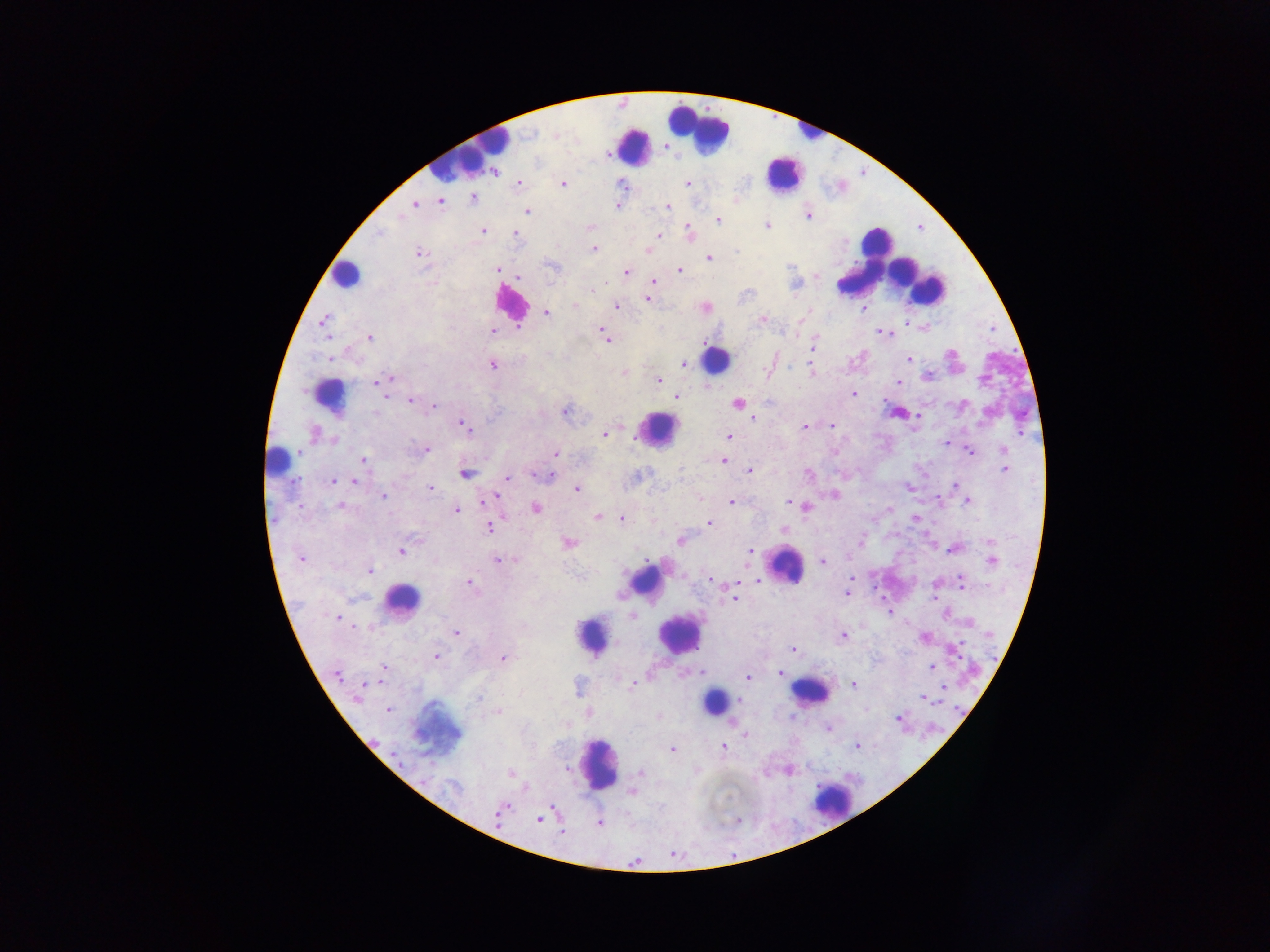
malaria parasite locations = approximate centers as (x, y) in pixels: (556, 135), (518, 183), (563, 183), (621, 183), (688, 183), (473, 198), (440, 202), (414, 204), (617, 206), (667, 207), (527, 211), (400, 216), (808, 216), (718, 220), (766, 225), (482, 231), (689, 232), (379, 233), (515, 234), (658, 236), (594, 248), (647, 251), (736, 251), (420, 253), (709, 258), (552, 266), (498, 270), (679, 270), (626, 272), (816, 276), (520, 277), (654, 281), (796, 284), (593, 290), (647, 300), (575, 305), (617, 307), (862, 309), (546, 313), (323, 320), (762, 320), (494, 331), (603, 331), (879, 331), (606, 337), (370, 338), (814, 345), (330, 358), (907, 359), (684, 363), (492, 365), (810, 369), (623, 372), (926, 376), (391, 378), (659, 380), (377, 382), (899, 382), (853, 394), (386, 397), (677, 397), (410, 400), (737, 403), (434, 405), (960, 406), (375, 412), (565, 412), (748, 416), (753, 418), (832, 425), (464, 426), (804, 427), (314, 434), (604, 434), (729, 436), (334, 440), (946, 442), (1004, 449), (426, 450), (970, 451), (299, 452), (834, 452), (556, 453), (364, 459), (724, 461), (1004, 469), (749, 470), (465, 474), (809, 474), (536, 476), (547, 476), (356, 478), (508, 478), (333, 480), (354, 481), (955, 485), (908, 487), (430, 489), (577, 489), (834, 494), (383, 497), (493, 497), (938, 500), (731, 501), (968, 501), (788, 503), (300, 506), (340, 506), (806, 508), (536, 509), (889, 509), (456, 510), (598, 517), (915, 518), (622, 519), (709, 523), (489, 527), (783, 530), (416, 540), (680, 540), (862, 540), (989, 541), (569, 543), (952, 549), (401, 552), (749, 552), (301, 559), (498, 560), (515, 560), (991, 560), (823, 562), (369, 571), (852, 578), (710, 580), (758, 582), (470, 583), (961, 583), (847, 592), (933, 597), (733, 600), (889, 613), (632, 616), (338, 618), (456, 633), (843, 635), (924, 637), (792, 649), (435, 657), (503, 658), (384, 667), (931, 667), (702, 672), (779, 674), (338, 675), (748, 677), (362, 685), (632, 685), (853, 685), (943, 687), (357, 698), (478, 698), (924, 699), (742, 701), (388, 710), (498, 712), (659, 717), (899, 718), (829, 729), (745, 734), (857, 746), (723, 747), (672, 749), (568, 769), (640, 772), (510, 774), (637, 777), (426, 779), (453, 786), (632, 792), (505, 806), (501, 811), (539, 819), (599, 823), (561, 831)
image size = 1270×952 pixels
field of view = single
preparation = thick blood film
country = Ghana
capture = mobile-phone photograph through a microscope
leukocyte locations = approximate centers as (x, y) in pixels (subset; some below the resolvable size): (805, 126), (697, 129), (632, 147), (465, 153), (782, 174), (877, 250), (882, 259), (346, 275), (928, 288), (511, 304), (716, 360), (329, 395), (658, 430), (277, 460), (785, 565), (645, 582), (401, 599), (678, 634), (592, 635), (809, 692), (714, 701), (435, 730), (601, 764), (831, 802)